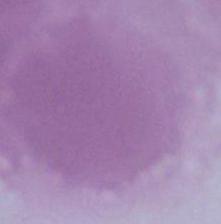

modality = photomicrograph
identification = red blood cell
magnification = 1000x